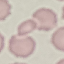
malaria status = uninfected
capture = smartphone through the microscope eyepiece
preparation = thin blood film
image type = cell patch, automatically extracted from a larger field of view and resized to 64 × 64 pixels
stain = Giemsa